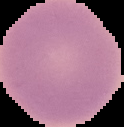

image type = cell region segmented out of the field of view; surrounding area masked to black
preparation = thin blood film
malaria status = uninfected
image size = 124×127 pixels